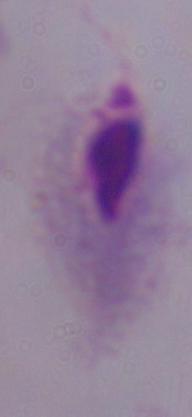

Summary:
  - Modality: photomicrograph
  - Identification: trichomonad
  - Magnification: 1000x